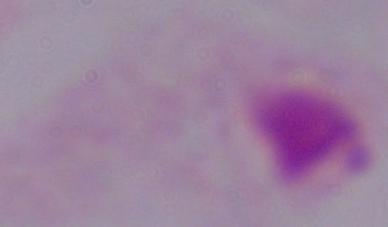

magnification = 1000x
modality = photomicrograph
identification = trichomonad